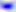 Toxoplasma gondii is shown. Photomicrograph. 400x magnification.